Locate every uninfected red blood cell.
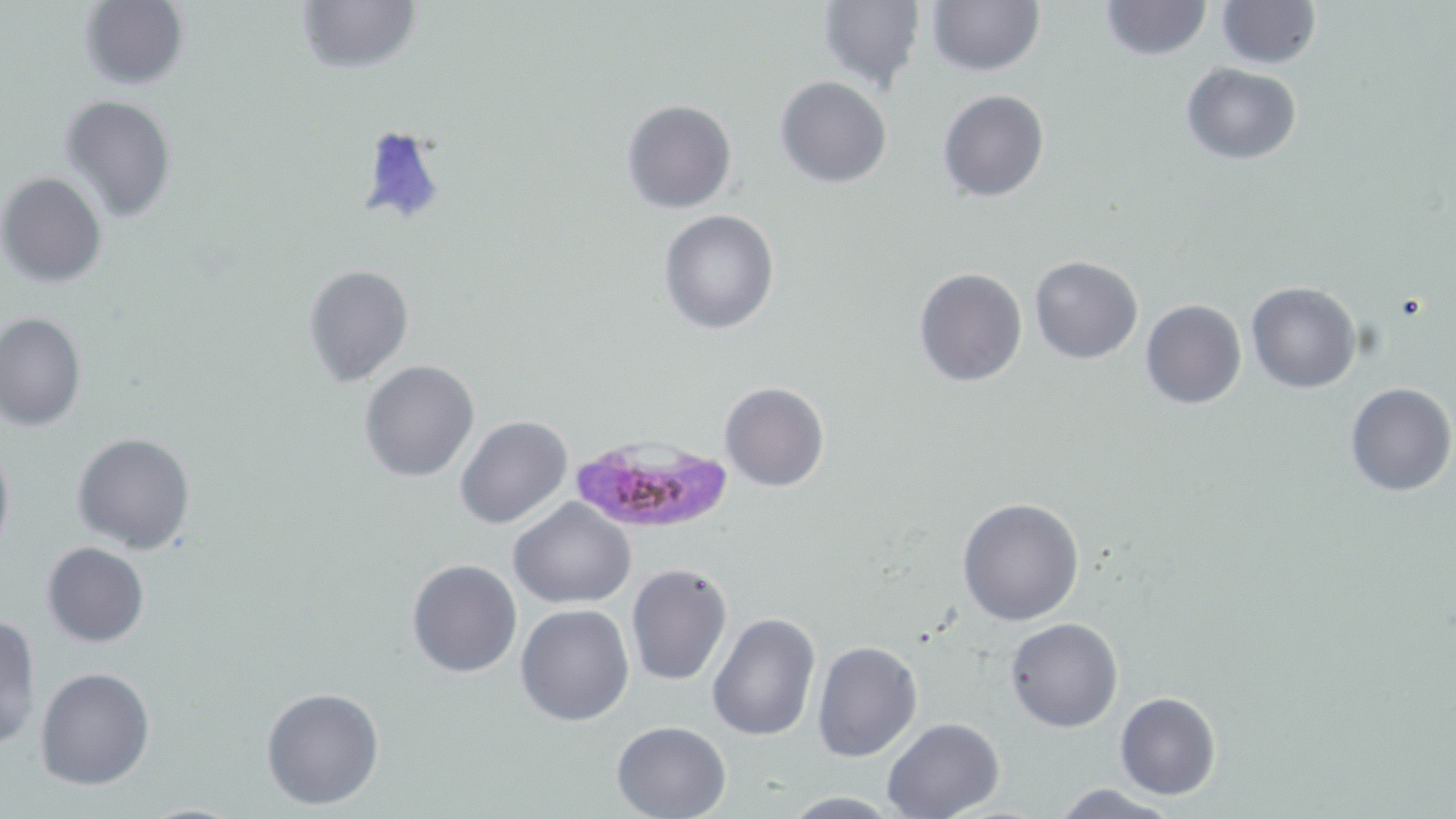

Approximate bounding boxes as (x1,y1)-(x2,y2) corner pairs in pixels.
Uninfected red blood cells: (294,0)-(420,76), (816,0)-(926,94), (926,0)-(1044,75), (79,1)-(189,91), (1098,1)-(1213,61), (1216,1)-(1321,70), (1181,62)-(1302,164), (775,76)-(891,188), (937,89)-(1050,202), (60,95)-(178,224), (622,99)-(737,216), (354,124)-(450,230), (0,172)-(107,286), (658,210)-(779,334), (1029,255)-(1143,363), (302,263)-(414,387), (913,266)-(1028,387), (1246,282)-(1362,394), (1141,299)-(1247,410), (0,310)-(86,431), (359,359)-(481,482), (720,381)-(830,491), (1344,382)-(1455,497), (455,414)-(572,530), (72,432)-(197,555), (0,433)-(14,564), (957,497)-(1085,626), (509,498)-(637,606), (42,542)-(148,648), (406,557)-(522,678), (626,564)-(733,687), (516,604)-(635,727), (706,609)-(820,743), (0,614)-(40,748), (1005,617)-(1123,731), (812,640)-(923,762), (35,666)-(156,789), (260,685)-(385,811), (1115,692)-(1221,801), (881,718)-(1003,819), (611,720)-(732,817), (1046,783)-(1182,818), (776,792)-(908,818).

Summary:
  - Plasmodium falciparum-infected red blood cell locations: (569,430)-(734,535)
  - Slide-level diagnosis: Plasmodium falciparum
  - Preparation: thin blood smear
  - Stain: May-Grünwald-Giemsa
  - Field of view: single
  - Magnification: 1000x
  - Image size: 1456×819 pixels
  - Modality: light microscopy